State the preparation type.
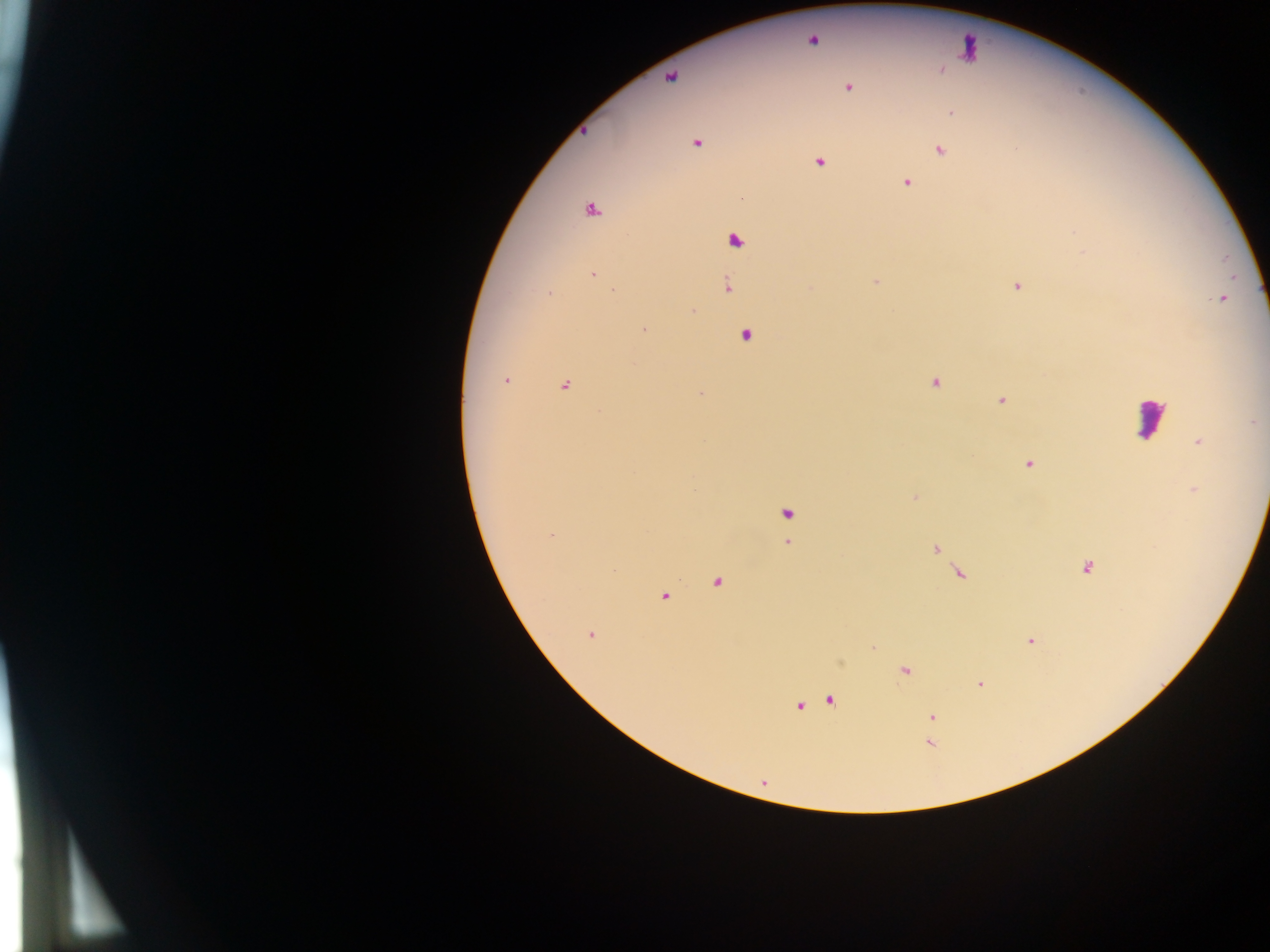

Thick blood smear.

Approximate centers as [x, y] in pixels. Malaria parasite locations: [812, 40], [670, 77], [848, 88], [952, 112], [697, 143], [940, 151], [820, 163], [907, 182], [591, 210], [735, 241], [593, 274], [876, 282], [727, 285], [1018, 286], [811, 288], [614, 291], [550, 293], [1222, 298], [692, 311], [644, 329], [745, 335], [506, 380], [935, 382], [565, 386], [700, 394], [1001, 400], [1254, 422], [1199, 442], [1028, 464], [915, 498], [787, 514], [551, 535], [788, 542], [936, 549], [1086, 568], [959, 574], [716, 583], [664, 597], [590, 634], [1030, 641], [904, 671], [980, 684], [831, 701], [799, 706], [932, 717], [930, 744]. Leukocyte locations: [968, 48], [1150, 418]. Single field of view. Image is 1270×952 pixels. Mobile-phone photograph taken through the microscope. Collected in Ghana.